Assess this cell for malaria.
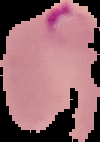

Parasitized.

Summary:
  - Image size: 100×142 pixels
  - Preparation: thin blood film
  - Image type: cell region segmented out of the field of view; surrounding area masked to black